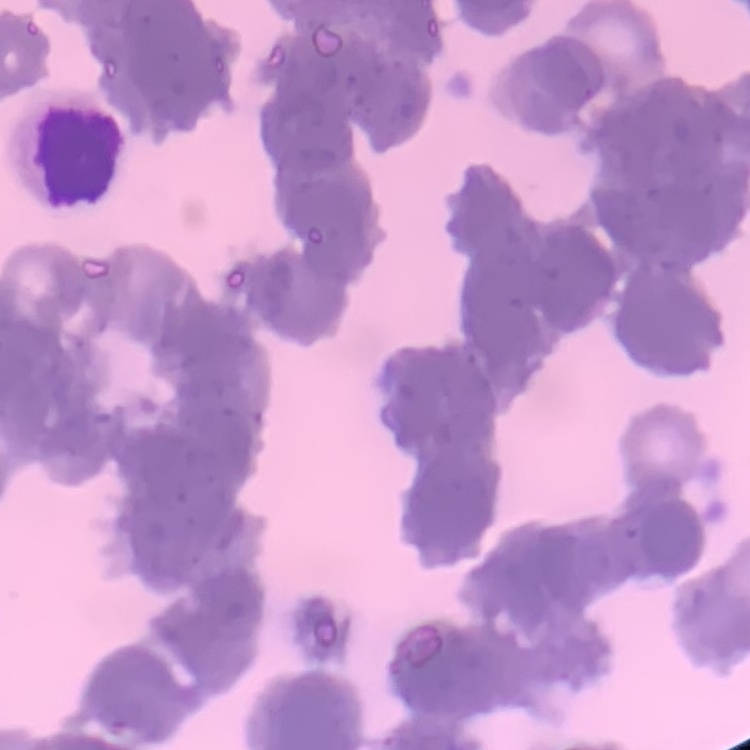

Summary:
  - Red blood cell morphology: rouleaux formation
  - Preparation: thin blood smear
  - Image type: square crop of a larger photomicrograph
  - Stain: Field's or Giemsa